Outline each blood parasite and name the species.
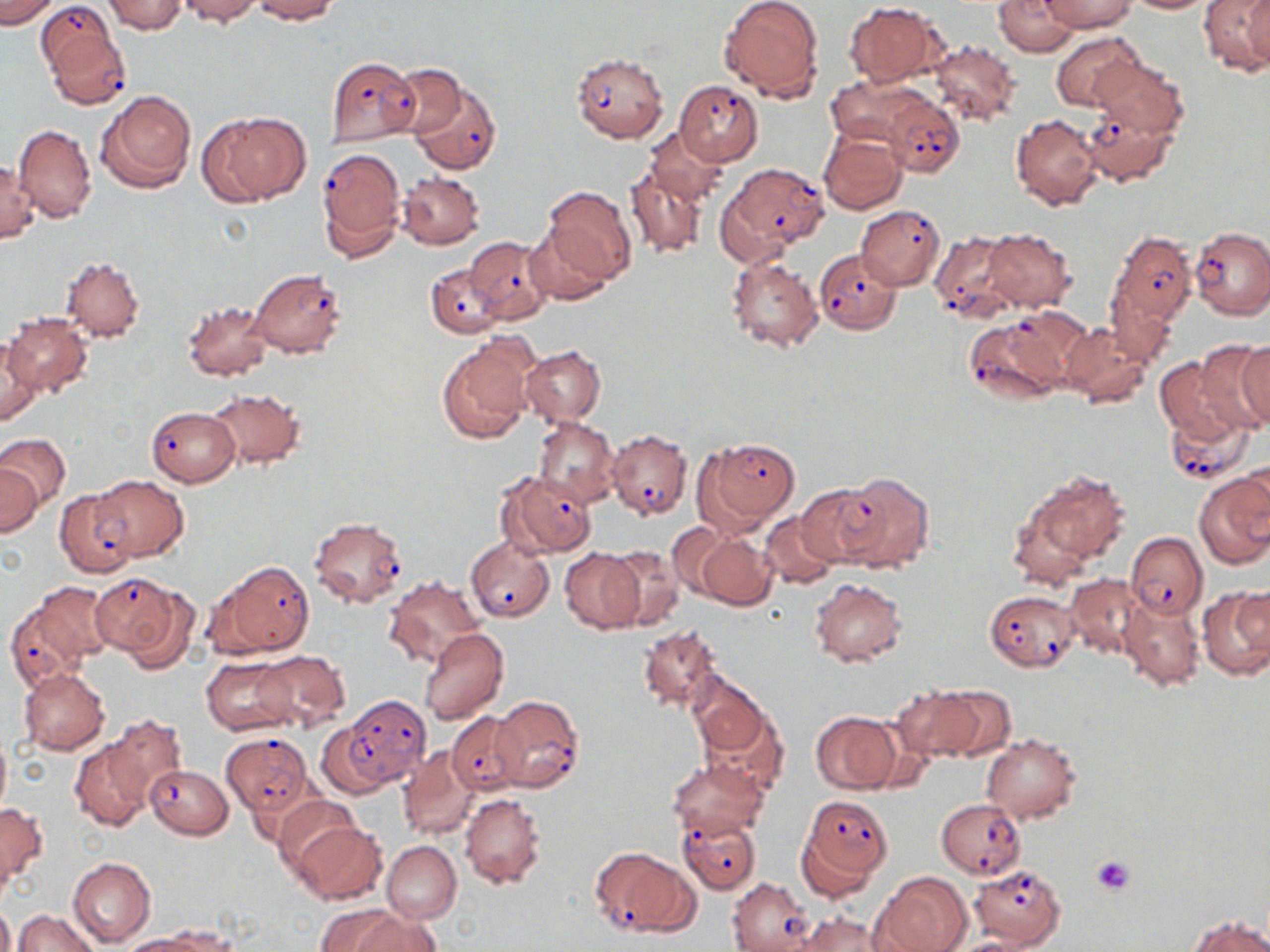

Approximate bounding boxes as (x1,y1)-(x2,y2) corner pairs in pixels.
Plasmodium falciparum-infected red blood cells: (37,1)-(118,80), (42,21)-(132,110), (571,52)-(668,141), (325,56)-(420,146), (409,79)-(501,174), (675,79)-(763,166), (882,95)-(964,178), (1081,105)-(1177,186), (317,148)-(406,259), (725,163)-(827,257), (855,205)-(945,289), (1189,226)-(1270,320), (928,228)-(1017,321), (1110,232)-(1197,326), (466,237)-(552,323), (815,249)-(904,334), (425,263)-(507,338), (248,269)-(345,357), (964,319)-(1069,405), (146,407)-(239,487), (1165,413)-(1254,487), (606,430)-(693,519), (698,437)-(799,533), (496,470)-(596,557), (91,474)-(187,561), (796,484)-(887,567), (308,517)-(408,608), (1126,532)-(1207,620), (465,537)-(554,622), (209,560)-(314,657), (92,572)-(193,667), (985,590)-(1080,672), (4,601)-(93,693), (490,694)-(585,793), (333,695)-(431,788), (446,711)-(527,794), (220,732)-(313,816), (145,765)-(233,839), (799,795)-(893,882), (936,798)-(1026,878), (678,813)-(761,895), (590,847)-(695,937), (970,864)-(1065,947), (728,877)-(813,951).
No Plasmodium ovale, Plasmodium malariae, Plasmodium vivax, Babesia divergens, or Trypanosoma brucei observed.

slide-level diagnosis = Plasmodium falciparum
stain = May-Grünwald-Giemsa
modality = optical microscopy
uninfected red blood cell locations = approximate bounding boxes as (x1,y1)-(x2,y2) corner pairs in pixels: (0,0)-(58,28), (102,0)-(187,34), (176,0)-(262,24), (250,0)-(339,22), (719,0)-(825,103), (995,0)-(1079,57), (1040,0)-(1138,32), (1121,0)-(1216,14), (1199,1)-(1270,75), (844,2)-(944,88), (1052,32)-(1145,113), (926,39)-(1021,126), (1089,53)-(1189,143), (385,62)-(467,141), (826,74)-(925,147), (98,90)-(195,192), (208,111)-(310,204), (1011,113)-(1104,212), (12,123)-(96,222), (644,126)-(731,206), (819,131)-(906,215), (1,158)-(40,243), (622,162)-(708,260), (397,171)-(483,249), (545,186)-(636,286), (523,224)-(613,305), (982,227)-(1076,311), (724,253)-(824,353), (61,256)-(144,341), (1107,284)-(1181,365), (182,298)-(274,382), (2,312)-(91,397), (1060,322)-(1152,407), (437,334)-(538,443), (0,338)-(44,427), (1223,341)-(1270,430), (519,345)-(606,427), (1154,355)-(1251,446), (208,388)-(304,470), (533,418)-(618,505), (0,434)-(70,508), (1240,462)-(1270,540), (0,465)-(42,538), (1017,470)-(1130,586), (1194,470)-(1270,569), (833,472)-(935,575), (55,489)-(137,578), (761,511)-(843,589), (666,522)-(742,601), (695,532)-(779,610), (607,545)-(685,632), (560,549)-(643,634), (1065,574)-(1146,659), (385,577)-(483,667), (808,579)-(907,667), (24,581)-(114,672), (1198,586)-(1270,680), (1118,594)-(1205,690), (638,624)-(723,711), (418,627)-(509,726), (251,649)-(349,733), (201,656)-(297,735), (19,667)-(110,754), (687,672)-(769,759), (937,684)-(1016,760), (891,686)-(985,763), (697,694)-(789,796), (811,712)-(899,793), (104,715)-(186,807), (316,718)-(399,797), (0,729)-(11,822), (982,733)-(1081,823), (71,739)-(153,831), (397,746)-(481,840), (666,755)-(769,839), (460,793)-(547,889), (273,795)-(364,877), (0,803)-(47,886), (290,819)-(387,905), (382,841)-(461,923), (68,856)-(156,947), (873,871)-(972,952), (0,900)-(14,952), (12,910)-(101,952), (792,911)-(885,952), (342,912)-(441,952), (1189,914)-(1269,951), (119,934)-(212,952)
image size = 1270×952 pixels
preparation = thin blood smear
field of view = single
platelet locations = approximate bounding boxes as (x1,y1)-(x2,y2) corner pairs in pixels: (1091,854)-(1136,897)
magnification = 1000x